Comment on the morphology of the erythrocytes.
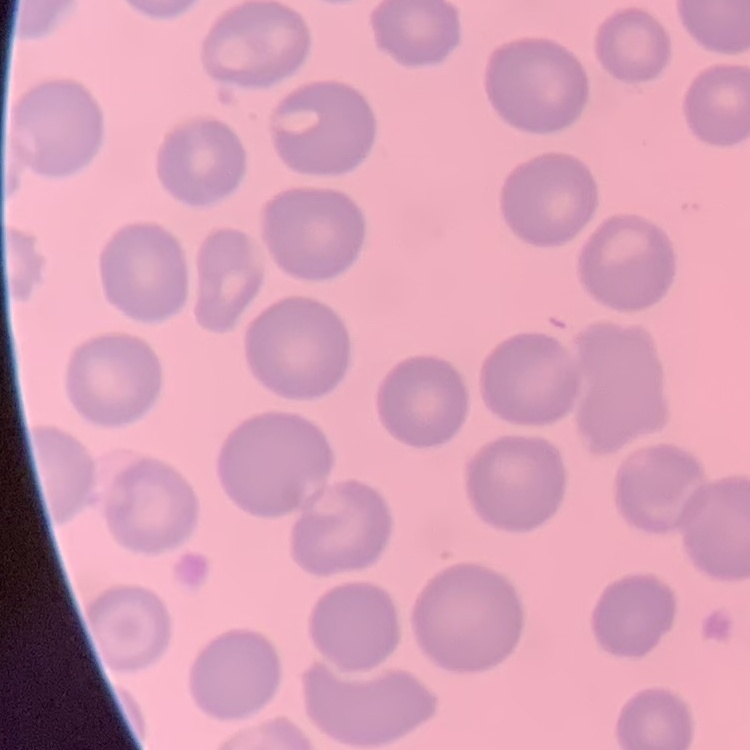

They show no rouleaux formation.

stain = Field's or Giemsa
image type = square crop of a larger photomicrograph
preparation = thin blood film